Identify the parasite.
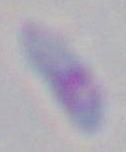

This is Toxoplasma gondii.

magnification = 1000x
modality = photomicrograph